Report the malaria status of this cell.
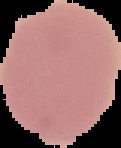

It is uninfected.

Image is 121×148 pixels. The area outside the segmented cell region is set to black. From a thin blood film.